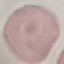 Malaria status: uninfected. Photographed with a smartphone camera at the microscope eyepiece. Thin smear of blood. Giemsa stain. Automatically extracted cell patch, resized to 64 × 64 pixels.